Classify this cell by malaria status.
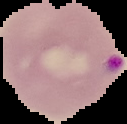
It is parasitized.

Summary:
  - Image size: 127×124 pixels
  - Preparation: thin blood smear
  - Image type: segmented cell region with the area outside set to black